Identify the parasite.
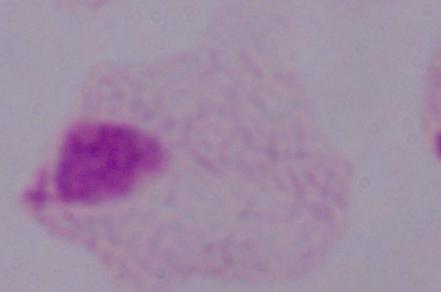

A trichomonad.

magnification: 1000x
modality: micrograph